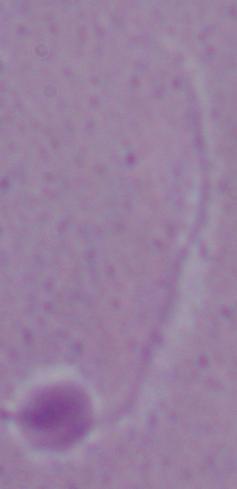
A Leishmania parasite is shown. Micrograph. Captured at 1000x magnification.